Assess this cell for malaria.
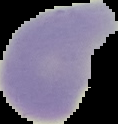

Uninfected.

Image is 118×124 pixels. From a thin blood smear. Segmented cell region on a black background.